Give the position of every Plasmodium parasite.
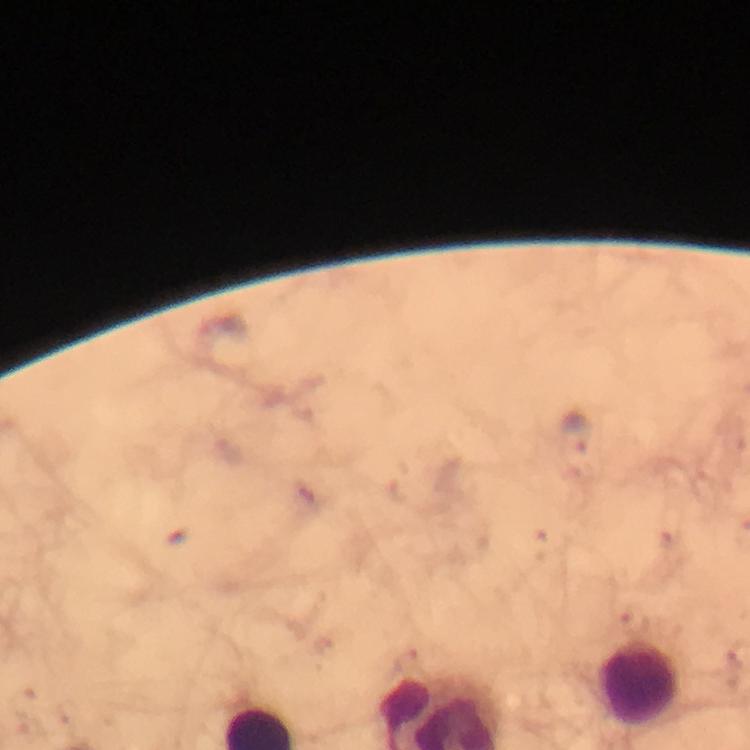
Approximate centers as {x, y} in pixels.
Plasmodium parasites: {577, 434}, {669, 541}, {632, 624}, {23, 703}.

Summary:
  - Leukocyte locations: {640, 684}
  - Cropped from: one field of view
  - Immersion oil: used
  - Preparation: thick smear
  - Magnification: 100x
  - Image size: 750×750 pixels
  - Capture: smartphone mounted on the microscope
  - Context: from a diagnostic examination for malaria
  - Stain: Giemsa